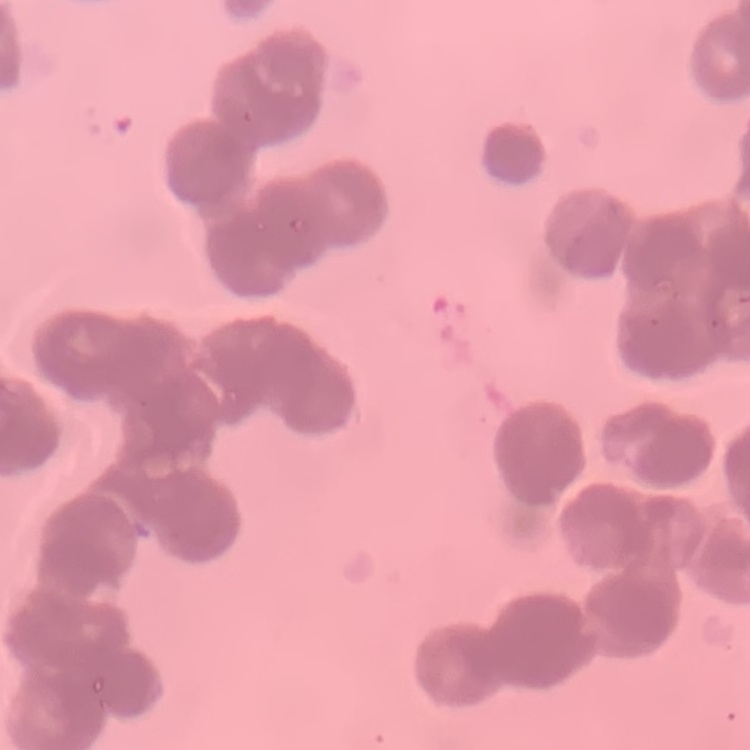
The erythrocytes show rouleaux formation. Thin blood film. Square crop of a larger photomicrograph. Field's or Giemsa stain.